Assess this cell for malaria.
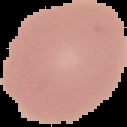

It is uninfected.

{
  "preparation": "thin blood smear",
  "image_size": "127×127 pixels",
  "image_type": "segmented cell region with the area outside set to black"
}